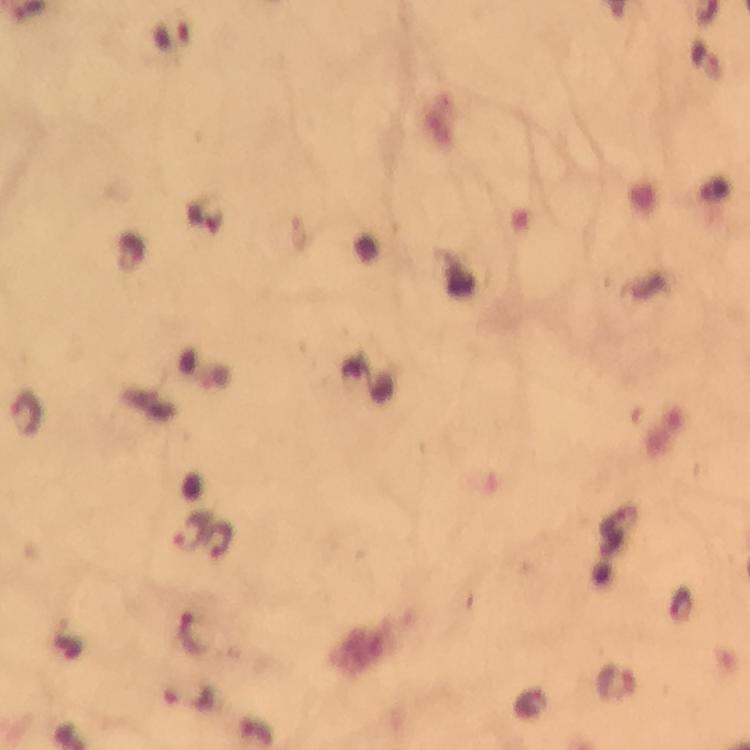

Approximate centers as (x, y) in pixels.
Summary:
  - Malaria parasite locations: (172, 36), (27, 413), (192, 532), (217, 535), (196, 634), (617, 683), (189, 700)
  - Capture: smartphone camera through the microscope
  - Magnification: 100x
  - Image size: 750×750 pixels
  - Immersion oil: used
  - Cropped from: a single field of view
  - Stain: Giemsa
  - Preparation: thick smear
  - Context: from a malaria diagnostic workup